Describe the morphology of the erythrocytes.
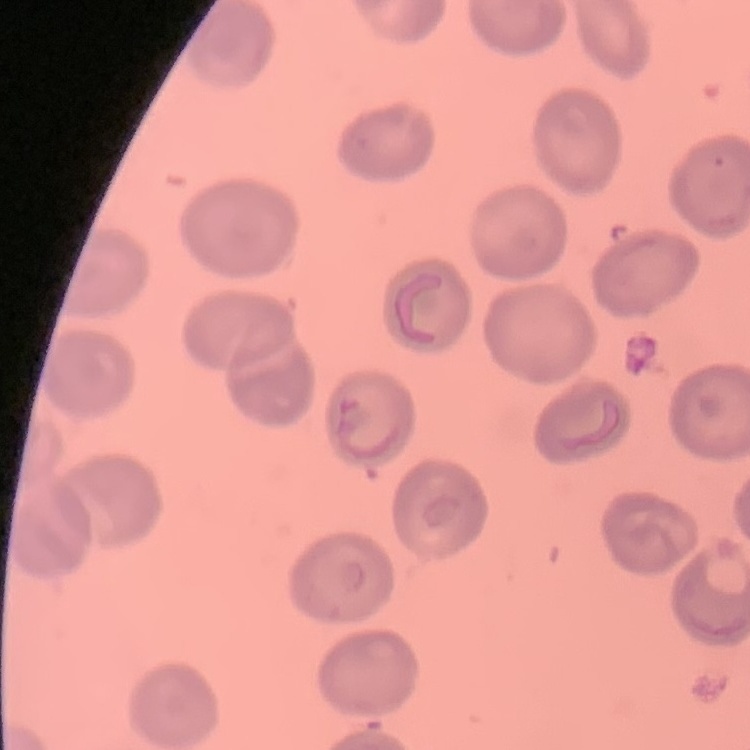
No rouleaux formation.

Summary:
  - Image type: square crop of a larger photomicrograph
  - Preparation: thin blood smear
  - Stain: Field's or Giemsa